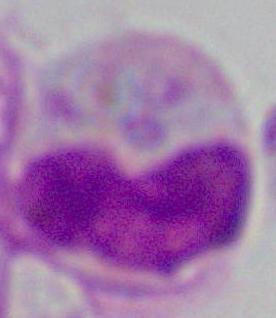
Photomicrograph. 1000x magnification. A white blood cell is shown.